Identify the parasite.
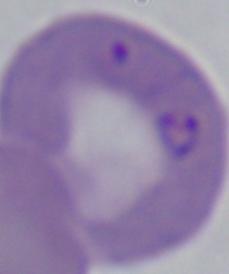
This is Babesia.

Micrograph. 1000x magnification.